Identify the blood parasite species.
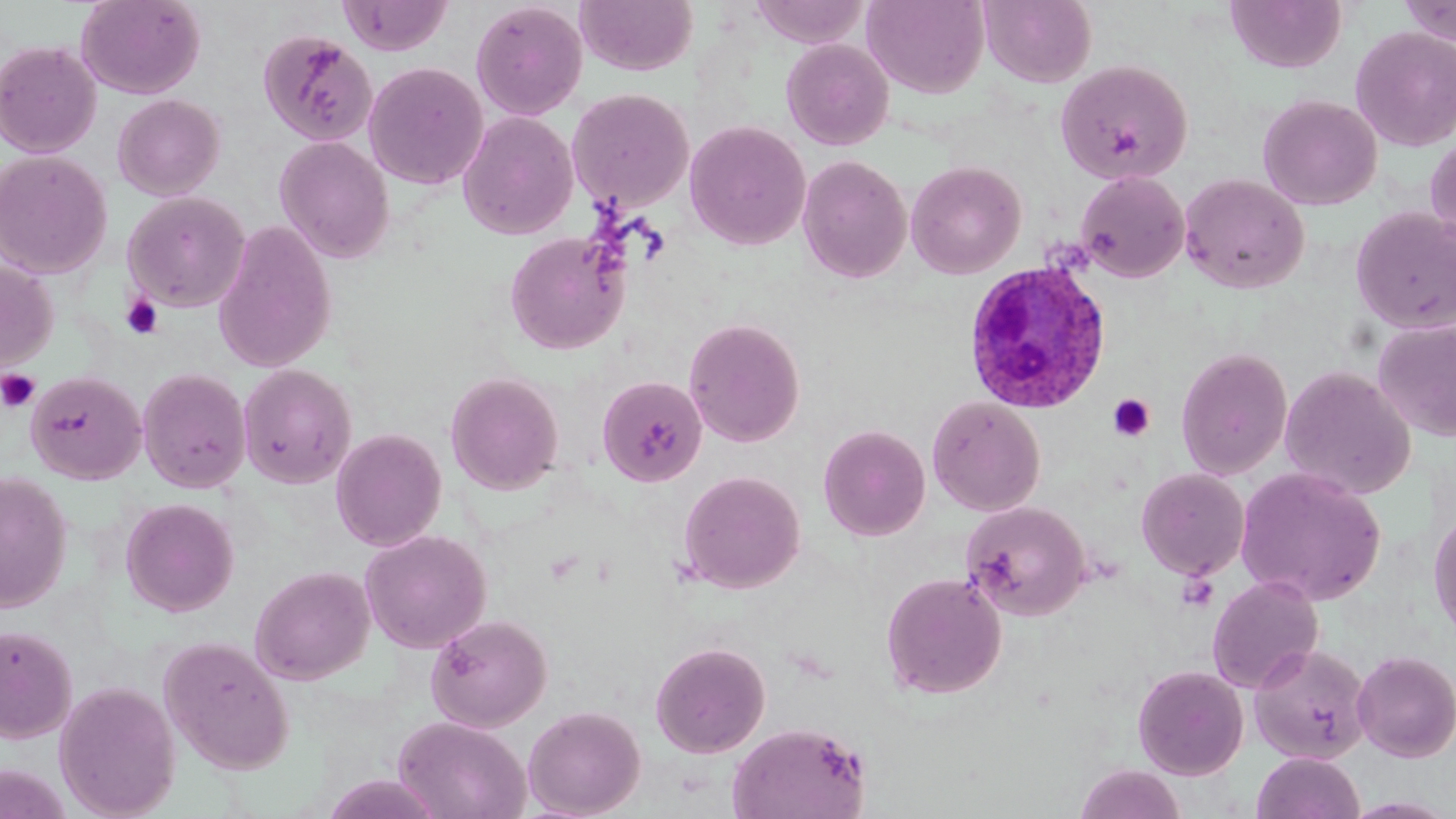
Plasmodium ovale.

Approximate bounding boxes as (x1,y1)-(x2,y2) corner pairs in pixels. Uninfected red blood cell locations: (76,0)-(205,99), (338,0)-(453,55), (575,0)-(698,76), (862,0)-(989,99), (981,0)-(1097,88), (1224,0)-(1347,74), (1397,0)-(1456,47), (749,1)-(869,48), (471,2)-(588,120), (1350,26)-(1456,152), (257,29)-(377,146), (781,38)-(894,150), (0,40)-(102,158), (1055,59)-(1193,185), (363,61)-(489,189), (567,88)-(694,212), (113,93)-(225,200), (1257,94)-(1382,211), (458,111)-(578,240), (684,120)-(811,250), (1425,134)-(1456,252), (274,136)-(395,263), (0,150)-(112,279), (797,154)-(912,284), (906,160)-(1027,279), (1075,170)-(1189,283), (1179,173)-(1310,294), (123,191)-(250,311), (1350,207)-(1456,335), (213,220)-(337,373), (505,231)-(629,354), (0,260)-(57,372), (1372,316)-(1456,441), (683,317)-(805,447), (1175,347)-(1293,480), (238,363)-(357,488), (1279,365)-(1417,500), (137,368)-(251,493), (25,370)-(145,484), (446,372)-(564,494), (596,376)-(708,487), (927,395)-(1046,516), (818,423)-(931,540), (330,427)-(447,551), (1136,467)-(1250,580), (1235,467)-(1386,606), (677,470)-(806,594), (0,471)-(72,613), (120,498)-(238,617), (961,501)-(1091,621), (1429,506)-(1456,642), (360,529)-(492,653), (250,564)-(375,684), (880,572)-(1007,699), (1207,575)-(1324,693), (426,614)-(552,732), (0,624)-(78,743), (158,636)-(295,775), (650,641)-(770,758), (1249,643)-(1373,764), (1353,650)-(1456,762), (1133,665)-(1248,780), (54,680)-(180,818), (523,705)-(646,818), (394,715)-(531,819), (727,720)-(872,819), (1252,752)-(1365,819), (1074,764)-(1186,819), (319,773)-(447,818). Plasmodium ovale-infected red blood cell locations: (962,260)-(1112,414). Platelet locations: (121,294)-(164,340), (0,369)-(41,413), (1108,394)-(1156,442). May-Grünwald-Giemsa-stained preparation. Image is 1456×819 pixels. 1000x magnification. Single field of view. Thin blood smear. Light microscopy.